Name the parasite shown.
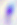

This is Toxoplasma gondii.

Photomicrograph. Captured at 400x magnification.